Give the extent of all uninfected red blood cells.
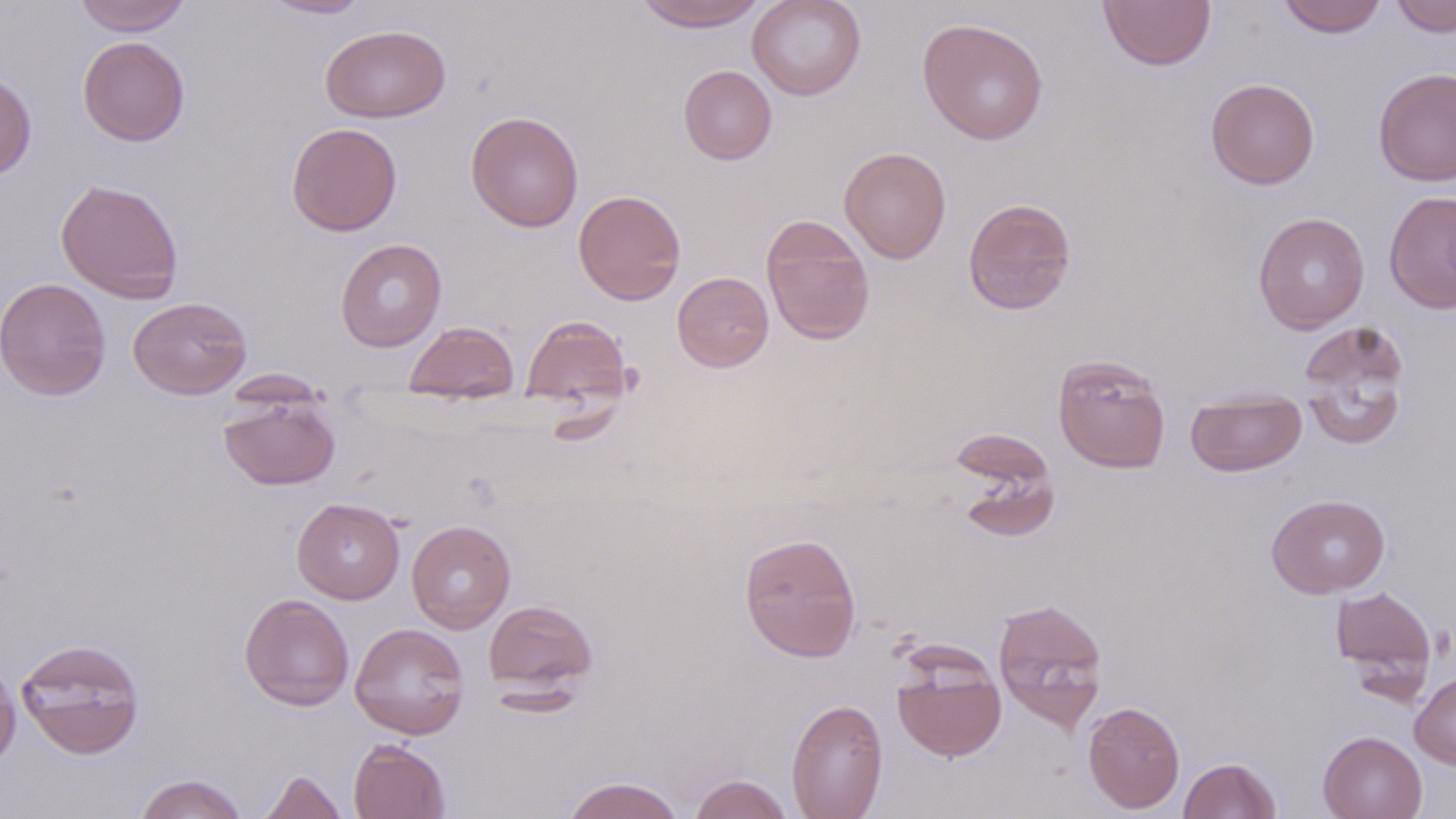
Approximate bounding boxes as (x1, y1, x2, y2) in pixels.
Uninfected red blood cells: (73, 0, 191, 35), (262, 0, 371, 19), (632, 0, 768, 32), (747, 0, 866, 100), (1098, 0, 1216, 71), (1277, 0, 1388, 38), (1390, 0, 1455, 37), (917, 18, 1048, 145), (319, 25, 451, 123), (78, 36, 190, 146), (678, 65, 777, 165), (1372, 66, 1456, 187), (0, 70, 37, 181), (1206, 78, 1320, 189), (466, 111, 584, 233), (286, 122, 403, 236), (839, 146, 951, 263), (55, 179, 184, 303), (572, 189, 686, 305), (1383, 190, 1456, 314), (963, 197, 1076, 315), (1253, 211, 1370, 334), (760, 215, 876, 345), (335, 238, 447, 352), (672, 271, 774, 372), (0, 277, 111, 400), (128, 297, 251, 399), (521, 314, 634, 411), (404, 321, 519, 403), (1297, 321, 1412, 449), (1053, 354, 1171, 473), (1185, 389, 1306, 477), (218, 394, 340, 491), (952, 433, 1060, 543), (1266, 493, 1390, 598), (292, 498, 405, 604), (406, 520, 515, 634), (739, 532, 862, 662), (1330, 584, 1437, 688), (239, 592, 355, 711), (992, 597, 1109, 733), (483, 600, 598, 693), (349, 622, 470, 739), (15, 638, 145, 759), (892, 653, 1006, 761), (0, 660, 21, 769), (1410, 670, 1456, 770), (786, 698, 888, 819), (1082, 700, 1185, 814), (1318, 730, 1427, 819), (348, 738, 451, 819), (1178, 756, 1281, 818), (258, 768, 350, 819), (133, 773, 250, 819), (688, 773, 795, 818), (561, 776, 686, 819).

Slide-level diagnosis: negative for blood parasites. Thin blood film. May-Grünwald-Giemsa stain. Image is 1456×819 pixels. Captured at 1000x magnification. Single field of view. Light microscopy.